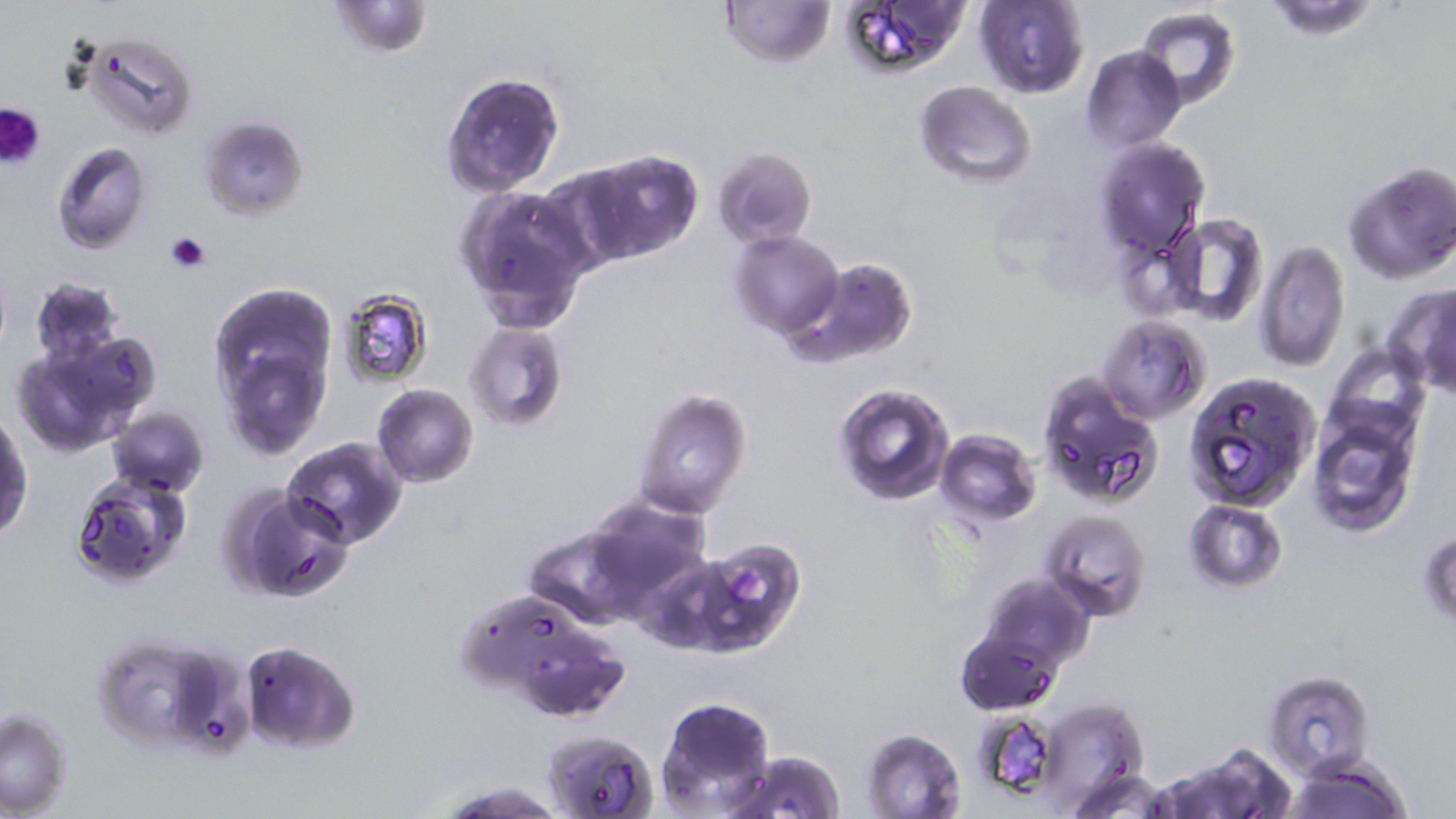
Summary:
  - Coordinate format: approximate bounding boxes as (x1, y1, x2, y2) in pixels
  - Platelet locations: (0, 102, 47, 169), (164, 232, 211, 272)
  - Uninfected red blood cell locations: (325, 0, 433, 58), (717, 0, 836, 70), (834, 0, 972, 82), (974, 1, 1090, 98), (1262, 1, 1380, 40), (1136, 6, 1240, 113), (77, 32, 199, 139), (1082, 45, 1185, 151), (440, 72, 565, 196), (914, 80, 1037, 186), (197, 115, 307, 220), (1095, 138, 1210, 261), (52, 142, 153, 254), (712, 146, 816, 248), (581, 147, 704, 264), (1341, 159, 1456, 283), (536, 160, 659, 269), (452, 183, 597, 334), (1163, 214, 1267, 328), (730, 230, 842, 338), (1255, 240, 1350, 372), (786, 256, 918, 368), (29, 277, 125, 368), (1387, 285, 1456, 394), (335, 288, 433, 388), (209, 289, 336, 457), (1099, 314, 1209, 423), (463, 321, 569, 433), (12, 335, 154, 458), (1324, 342, 1428, 448), (1034, 370, 1163, 508), (1186, 371, 1320, 511), (831, 383, 956, 504), (372, 384, 478, 487), (632, 386, 752, 520), (107, 407, 210, 498), (1309, 411, 1417, 536), (1, 413, 34, 541), (935, 430, 1041, 526), (282, 438, 407, 550), (69, 473, 191, 592), (226, 485, 353, 603), (584, 496, 711, 608), (1183, 500, 1289, 592), (1043, 510, 1151, 623), (523, 524, 643, 628), (1419, 529, 1455, 628), (687, 538, 805, 655), (974, 573, 1094, 675), (482, 607, 632, 726), (956, 627, 1062, 715), (92, 633, 223, 750), (239, 641, 360, 753), (1263, 670, 1375, 777), (655, 697, 778, 817), (1029, 697, 1150, 809), (0, 708, 74, 816), (970, 710, 1064, 802), (542, 728, 659, 818), (860, 728, 966, 818), (1167, 743, 1293, 819), (729, 749, 847, 819), (1286, 755, 1411, 819), (1068, 767, 1173, 818), (434, 776, 562, 816)
  - Slide-level diagnosis: Plasmodium falciparum
  - Magnification: 1000x
  - Image size: 1456×819 pixels
  - Preparation: thin blood film
  - Field of view: one of a larger specimen
  - Modality: light microscopy
  - Stain: May-Grünwald-Giemsa